Describe the morphology of the red blood cells.
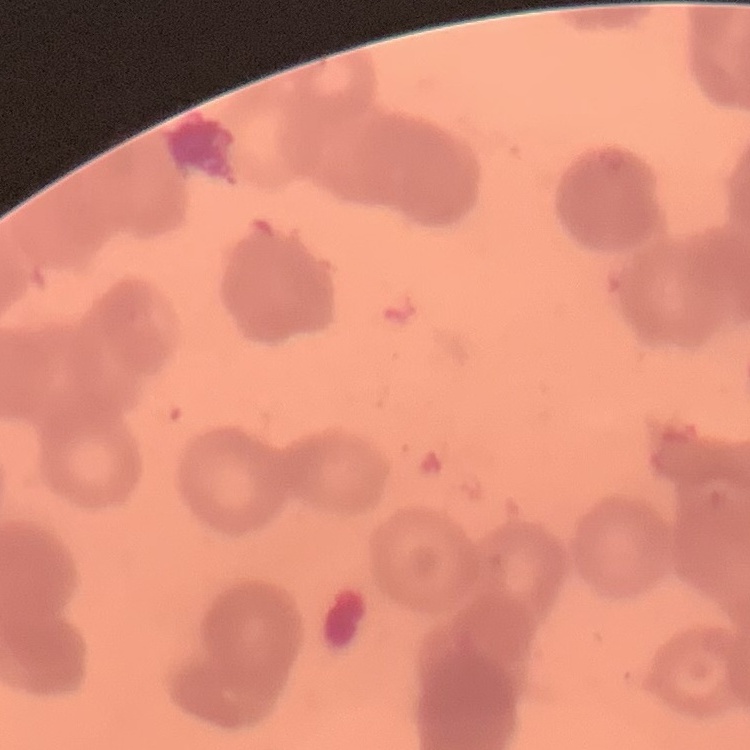

They show rouleaux formation.

Summary:
  - Image type: square crop of a larger photomicrograph
  - Stain: Field's or Giemsa
  - Preparation: thin blood film